Describe the morphology of the red blood cells.
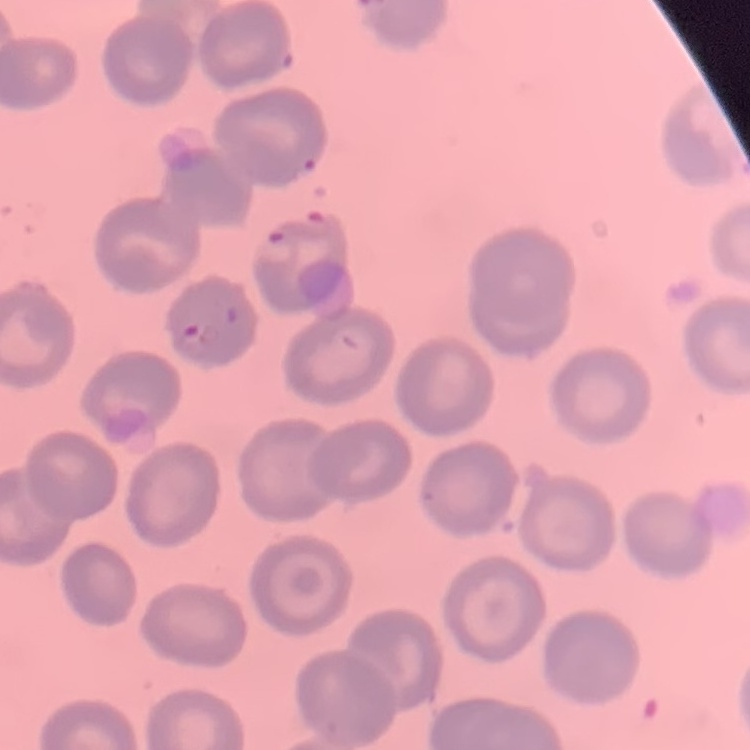

No rouleaux formation.

{
  "stain": "Field's or Giemsa",
  "image_type": "one tile cut from a larger photomicrograph",
  "preparation": "thin peripheral smear"
}